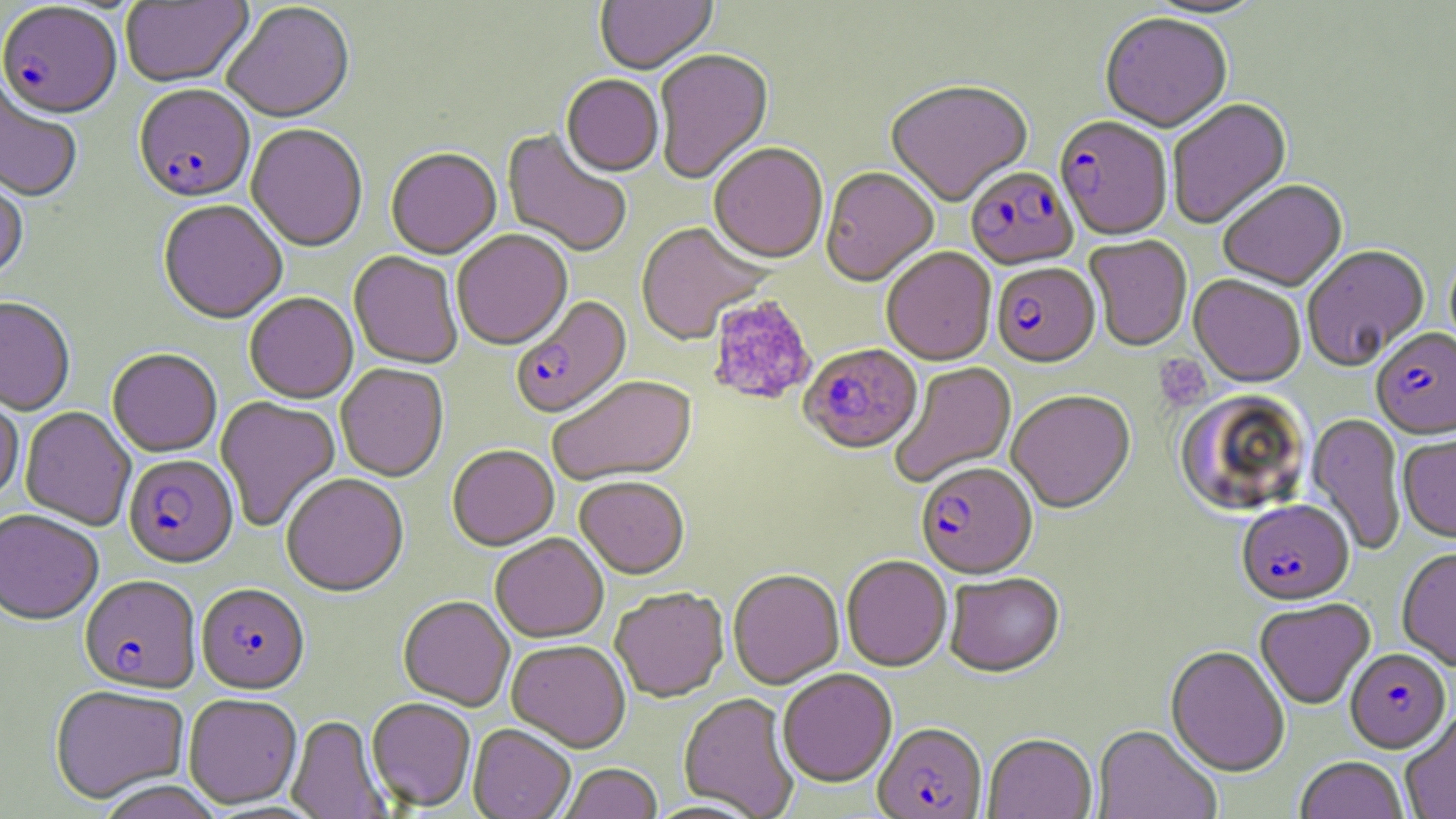
Approximate bounding boxes as [x1, y1, x2, y2] in pixels. Platelet locations: [706, 295, 818, 406], [1155, 354, 1212, 411]. Plasmodium falciparum-infected red blood cell locations: [0, 5, 122, 123], [133, 87, 255, 206], [1054, 118, 1172, 242], [966, 169, 1078, 272], [992, 265, 1100, 370], [511, 296, 633, 422], [1371, 330, 1456, 442], [799, 345, 922, 457], [123, 456, 238, 571], [916, 464, 1037, 581], [1236, 501, 1354, 607], [79, 577, 201, 696], [196, 585, 309, 697], [1344, 649, 1451, 754], [873, 725, 988, 819]. Uninfected red blood cell locations: [595, 0, 717, 76], [1142, 0, 1268, 20], [120, 1, 254, 90], [223, 3, 356, 126], [1101, 15, 1231, 135], [654, 51, 774, 185], [560, 76, 663, 179], [0, 82, 82, 204], [886, 83, 1033, 208], [1168, 99, 1293, 231], [246, 125, 367, 254], [502, 129, 631, 258], [709, 144, 828, 266], [386, 150, 502, 261], [820, 169, 938, 289], [0, 176, 28, 286], [1218, 182, 1348, 294], [158, 202, 287, 326], [635, 223, 768, 347], [452, 231, 573, 352], [1085, 237, 1192, 352], [1303, 246, 1430, 372], [882, 249, 997, 367], [349, 253, 463, 370], [1189, 276, 1305, 389], [244, 294, 358, 406], [0, 300, 75, 416], [107, 350, 222, 458], [890, 362, 1018, 488], [336, 364, 448, 483], [550, 377, 699, 488], [0, 389, 24, 506], [1173, 391, 1314, 519], [1007, 392, 1136, 515], [215, 397, 341, 532], [20, 406, 136, 532], [1306, 413, 1406, 556], [1398, 432, 1456, 545], [447, 447, 559, 553], [281, 476, 409, 599], [574, 478, 689, 580], [0, 511, 103, 628], [491, 534, 609, 645], [1397, 549, 1456, 672], [841, 557, 952, 672], [728, 571, 844, 690], [945, 574, 1065, 680], [611, 589, 729, 704], [398, 597, 515, 712], [1255, 600, 1375, 710], [506, 641, 630, 753], [1165, 647, 1290, 778], [777, 670, 896, 789], [50, 687, 189, 805], [679, 694, 800, 818], [184, 695, 302, 809], [366, 698, 476, 812], [1401, 712, 1455, 819], [287, 716, 391, 819], [468, 726, 575, 819], [1092, 726, 1222, 819], [983, 735, 1097, 819], [1295, 757, 1409, 819], [560, 765, 662, 819], [98, 780, 221, 819]. Slide-level diagnosis: Plasmodium falciparum. May-Grünwald-Giemsa-stained preparation. One field of a larger specimen. Captured at 1000x magnification. Thin blood film. Image is 1456×819 pixels. Light microscopy.